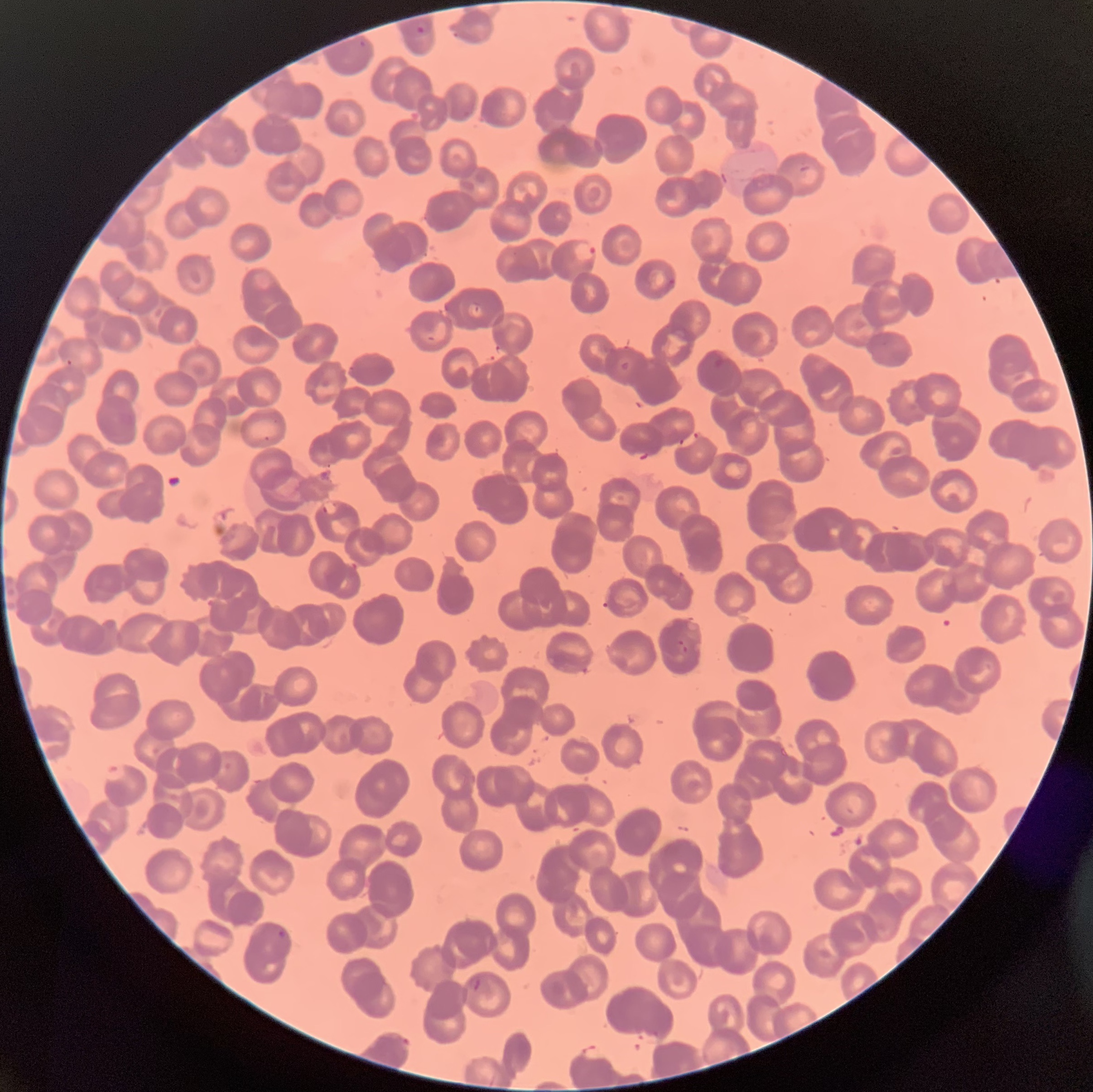

Summary:
  - Coordinate format: approximate bounding boxes as named x1/y1/x2/y2 corners in pixels
  - Plasmodium parasite locations: (x1=415, y1=25, x2=427, y2=37), (x1=358, y1=39, x2=368, y2=49), (x1=573, y1=241, x2=596, y2=263), (x1=660, y1=278, x2=675, y2=294), (x1=713, y1=355, x2=727, y2=369), (x1=66, y1=358, x2=74, y2=366), (x1=620, y1=361, x2=631, y2=372), (x1=321, y1=501, x2=339, y2=515), (x1=676, y1=639, x2=689, y2=654), (x1=103, y1=763, x2=130, y2=783), (x1=277, y1=929, x2=287, y2=941), (x1=469, y1=975, x2=493, y2=995), (x1=399, y1=1036, x2=414, y2=1052)
  - Modality: light microscopy
  - Image size: 1093×1092 pixels
  - Preparation: thin blood film
  - Red blood cell morphology: rouleaux formation